Identify the cell.
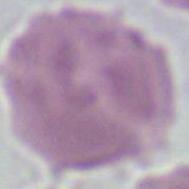

This is an erythrocyte.

magnification = 1000x
modality = micrograph